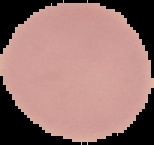
Summary:
  - Image type: segmented cell region with the area outside set to black
  - Image size: 154×145 pixels
  - Result: no Plasmodium parasites seen
  - Preparation: thin blood film